Assess this cell for malaria.
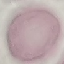
It is uninfected.

Photographed with a smartphone camera at the microscope eyepiece. Thin blood film. Automatically extracted cell patch, resized to 64 × 64 pixels. Giemsa stain.